Give the extent of all Plasmodium vivax-infected red blood cells.
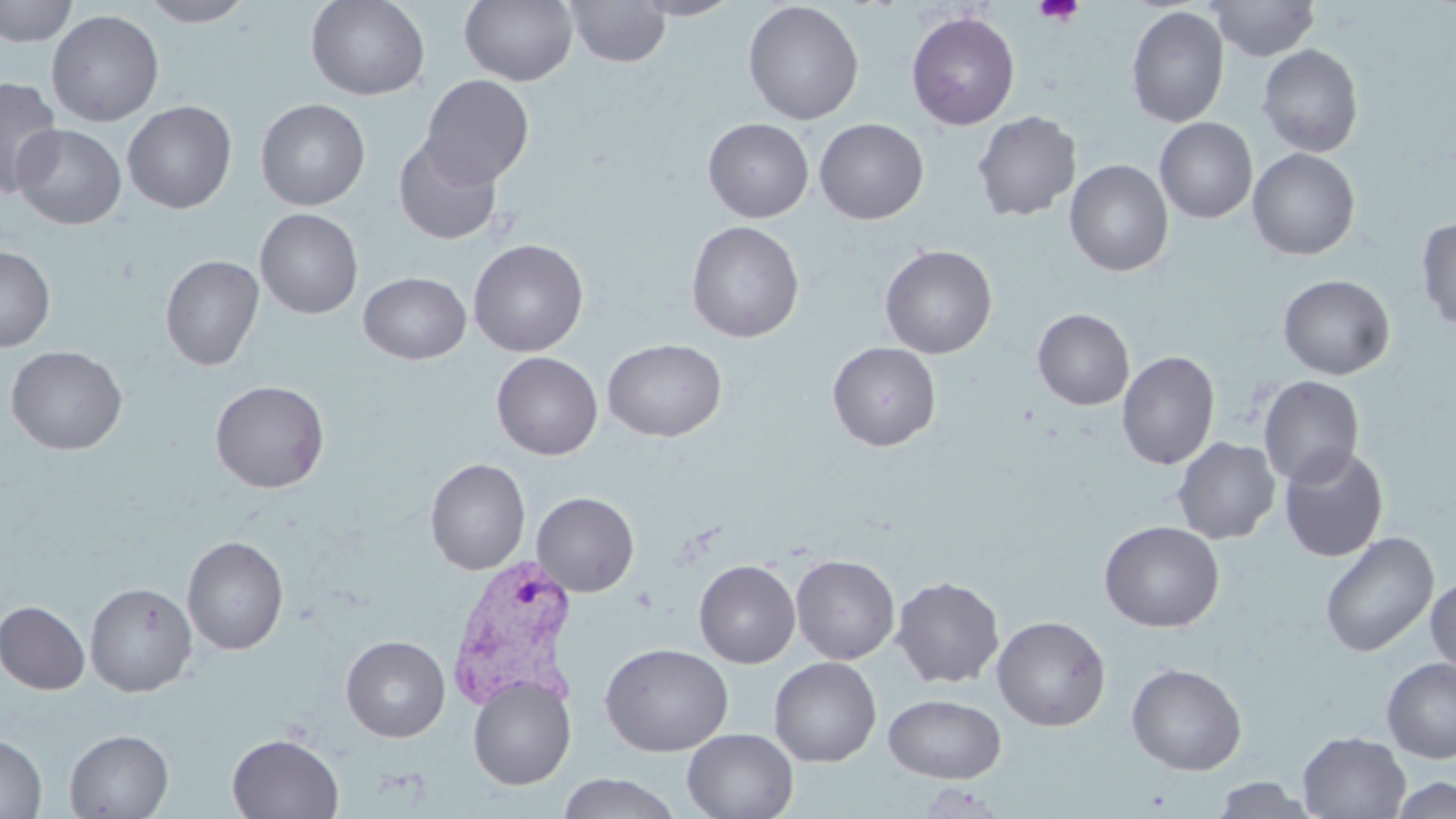

Approximate bounding boxes as (x1, y1, x2, y2) in pixels.
Plasmodium vivax-infected red blood cells: (446, 554, 581, 712).

slide_level_diagnosis: Plasmodium vivax
magnification: 1000x
modality: optical microscopy
uninfected_red_blood_cell_locations: 'approximate bounding boxes as (x1, y1, x2, y2) in pixels: (138, 0, 255, 27), (305, 0, 430, 101), (459, 0, 578, 86), (565, 0, 671, 68), (630, 0, 741, 20), (1210, 0, 1319, 60), (0, 1, 77, 47), (743, 1, 864, 125), (1126, 5, 1230, 128), (47, 9, 164, 127), (905, 10, 1020, 131), (1256, 44, 1364, 157), (420, 74, 534, 188), (0, 76, 63, 198), (256, 98, 370, 210), (122, 100, 237, 214), (971, 110, 1081, 222), (1154, 117, 1258, 223), (702, 118, 814, 222), (814, 118, 928, 224), (11, 123, 126, 230), (393, 135, 502, 245), (1247, 148, 1360, 260), (1064, 159, 1173, 277), (255, 208, 363, 319), (1415, 216, 1456, 332), (685, 220, 805, 342), (468, 238, 589, 357), (879, 244, 997, 358), (0, 245, 55, 352), (160, 254, 264, 371), (358, 271, 471, 364), (1277, 274, 1395, 379), (1032, 308, 1134, 410), (602, 338, 727, 441), (827, 342, 941, 451), (5, 345, 127, 455), (1117, 351, 1220, 470), (491, 352, 603, 460), (1258, 376, 1364, 487), (209, 380, 330, 493), (1172, 437, 1280, 544), (1278, 445, 1389, 563), (425, 458, 530, 575), (531, 492, 640, 596), (1099, 521, 1225, 632), (1319, 531, 1438, 657), (182, 536, 288, 655), (790, 554, 900, 665), (694, 560, 800, 668), (891, 576, 1005, 688), (1426, 576, 1456, 677), (85, 582, 197, 696), (1, 601, 90, 694), (991, 615, 1110, 731), (341, 634, 450, 742), (600, 642, 733, 756), (768, 656, 881, 767), (1381, 657, 1456, 764), (1126, 662, 1246, 775), (468, 674, 576, 790), (884, 694, 1006, 783), (64, 729, 174, 818), (682, 729, 798, 818), (1297, 732, 1410, 818), (227, 733, 344, 818), (0, 734, 47, 818), (557, 772, 682, 818), (1210, 776, 1317, 818), (1389, 776, 1455, 818), (917, 783, 1009, 818)'
platelet_locations: 'approximate bounding boxes as (x1, y1, x2, y2) in pixels: (1033, 0, 1085, 26)'
stain: May-Grünwald-Giemsa
preparation: thin blood smear
image_size: 1456×819 pixels
field_of_view: single